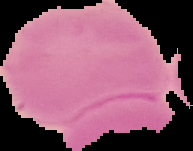

From a thin blood smear. The area outside the segmented cell region is set to black. Malaria status: uninfected. Image is 193×151 pixels.